Comment on the morphology of the red blood cells.
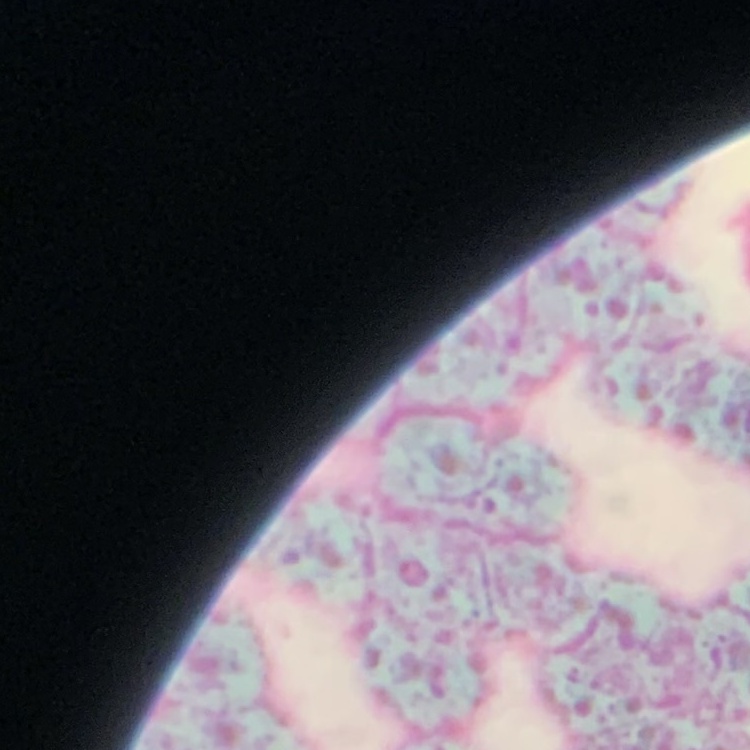
They show rouleaux formation.

stain = Field's or Giemsa
image type = square crop of a larger photomicrograph
preparation = thin blood smear